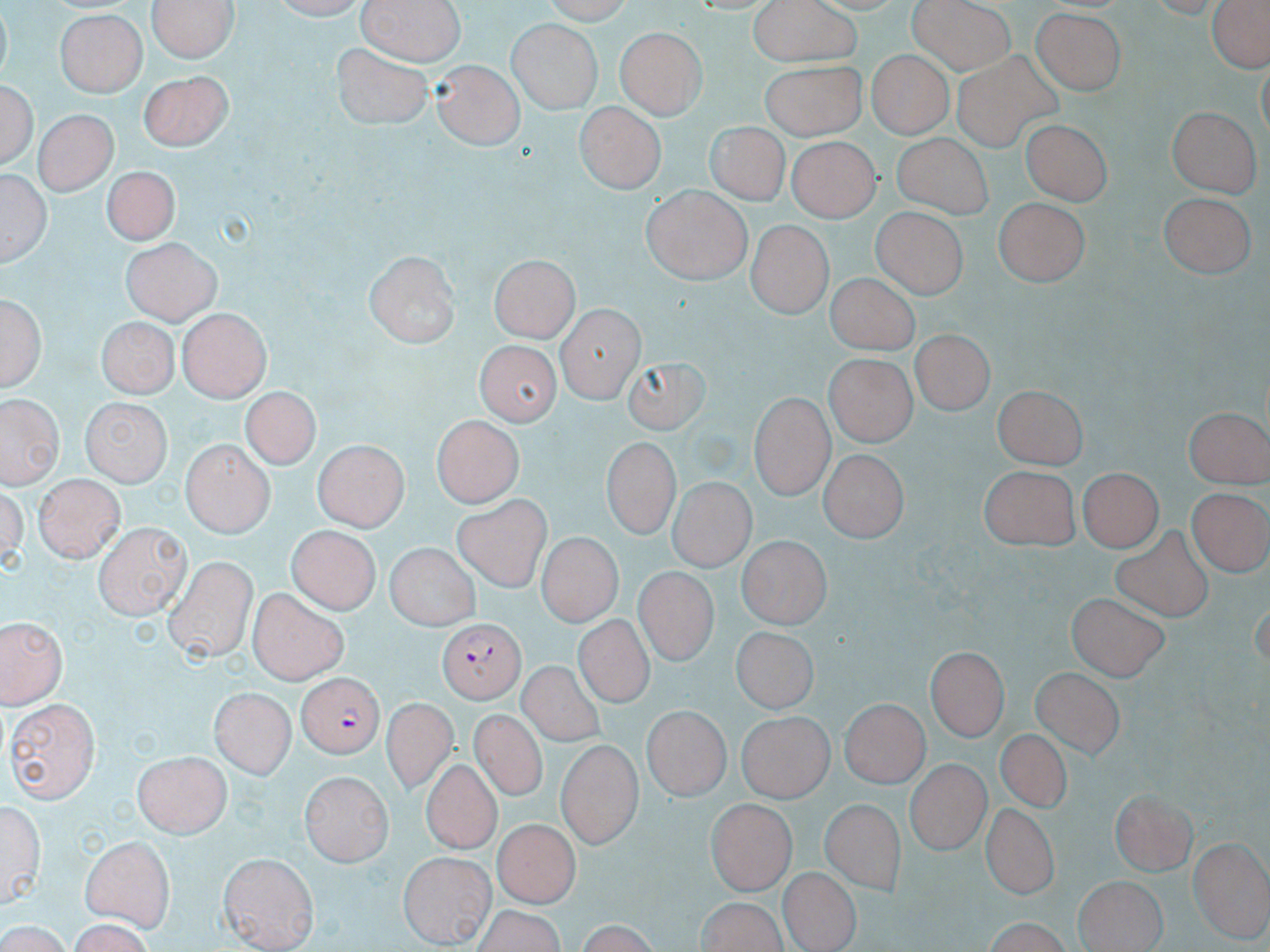

Summary:
  - Coordinate format: approximate bounding boxes as (x1,y1)-(x2,y2) corner pairs in pixels
  - Uninfected red blood cell locations: (150,0)-(237,63), (355,0)-(461,70), (748,0)-(862,68), (907,0)-(1013,73), (1205,0)-(1270,74), (1029,7)-(1129,99), (54,9)-(148,99), (509,20)-(600,111), (615,27)-(705,120), (330,41)-(436,131), (865,51)-(953,137), (944,52)-(1064,152), (430,60)-(520,152), (760,64)-(871,140), (140,70)-(234,151), (2,71)-(37,174), (573,105)-(663,196), (1168,106)-(1258,197), (35,110)-(116,195), (1023,116)-(1113,207), (701,121)-(795,207), (892,133)-(993,215), (785,134)-(877,223), (4,164)-(50,274), (105,165)-(176,246), (642,185)-(749,284), (1157,192)-(1254,279), (993,196)-(1091,289), (873,207)-(967,298), (746,220)-(831,318), (123,237)-(221,325), (364,248)-(459,349), (491,256)-(577,345), (826,273)-(921,353), (2,292)-(48,397), (555,306)-(642,400), (174,312)-(268,403), (94,320)-(175,400), (914,325)-(998,415), (467,338)-(568,434), (617,356)-(717,439), (825,356)-(915,446), (995,384)-(1086,468), (744,387)-(830,499), (238,389)-(321,473), (2,398)-(58,487), (80,398)-(170,485), (1185,401)-(1270,486), (430,415)-(526,508), (601,439)-(676,541), (181,441)-(275,539), (314,441)-(406,533), (817,451)-(905,542), (977,466)-(1081,549), (1079,468)-(1161,553), (36,475)-(121,559), (666,479)-(762,574), (1187,485)-(1266,579), (453,492)-(553,591), (96,521)-(191,616), (1110,524)-(1221,628), (288,527)-(376,613), (533,532)-(627,628), (738,535)-(830,632), (385,542)-(479,632), (162,557)-(254,659), (635,568)-(713,668), (249,590)-(351,683), (1065,595)-(1172,679), (0,615)-(67,709), (572,615)-(660,707), (729,626)-(813,714), (931,645)-(1009,736), (514,661)-(609,746), (1030,664)-(1133,761), (210,687)-(297,776), (840,697)-(928,789), (6,698)-(99,802), (380,699)-(457,792), (642,706)-(727,802), (467,709)-(552,801), (738,710)-(832,804), (555,736)-(642,848), (999,736)-(1081,808), (135,749)-(232,834), (906,758)-(988,857), (423,763)-(499,851), (300,770)-(395,863), (1110,788)-(1195,876), (2,798)-(46,912), (706,798)-(795,895), (819,799)-(903,895), (980,802)-(1057,902), (494,819)-(578,904), (77,832)-(179,930), (1187,838)-(1270,938), (219,853)-(318,951), (399,854)-(494,946), (778,867)-(858,950), (1074,875)-(1166,952), (695,895)-(795,952), (475,901)-(572,952), (57,920)-(156,950)
  - Plasmodium falciparum-infected red blood cell locations: (439,618)-(522,705), (293,673)-(387,756)
  - Slide-level diagnosis: Plasmodium falciparum
  - Magnification: 1000x
  - Stain: May-Grünwald-Giemsa
  - Modality: optical microscopy
  - Image size: 1270×952 pixels
  - Field of view: one of a larger specimen
  - Preparation: thin blood smear